Locate the Plasmodium falciparum-infected red blood cells and any of indeterminate infection status.
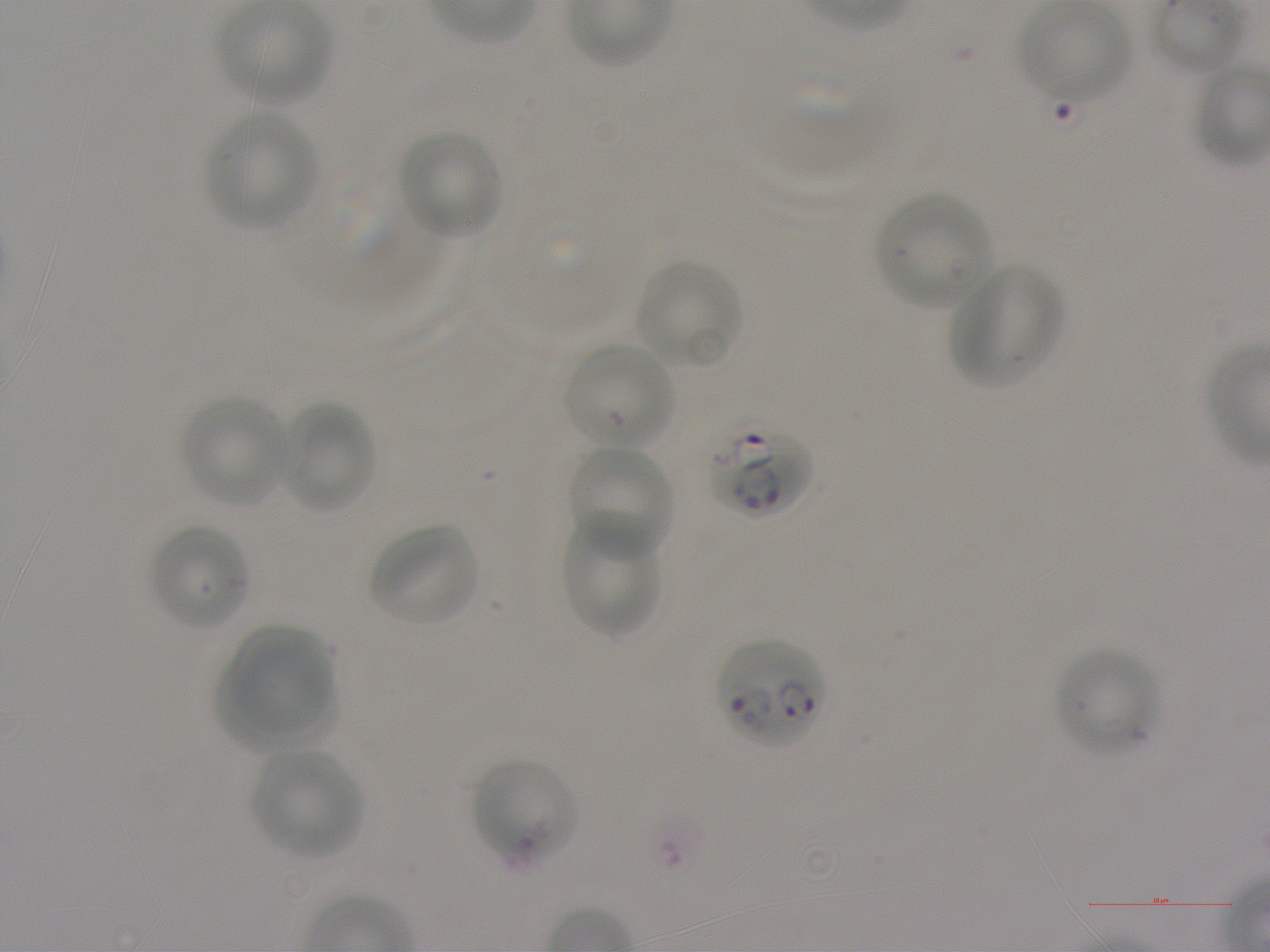
Approximate bounding rectangles given as corner coordinates in pixels from the top-left. Not every red blood cell is marked.
Infected red blood cells: (x1=706, y1=426, x2=813, y2=520), (x1=718, y1=639, x2=825, y2=750).
Red blood cells of indeterminate infection status: (x1=564, y1=344, x2=675, y2=451), (x1=472, y1=758, x2=578, y2=869).

Summary:
  - Locations of uninfected red blood cells: (x1=1019, y1=3, x2=1130, y2=104), (x1=217, y1=4, x2=329, y2=105), (x1=206, y1=112, x2=315, y2=231), (x1=397, y1=131, x2=501, y2=239), (x1=877, y1=193, x2=994, y2=309), (x1=635, y1=260, x2=743, y2=369), (x1=947, y1=266, x2=1064, y2=387), (x1=182, y1=396, x2=291, y2=507), (x1=280, y1=404, x2=377, y2=513), (x1=568, y1=441, x2=674, y2=560), (x1=564, y1=515, x2=661, y2=641), (x1=148, y1=523, x2=251, y2=631), (x1=369, y1=525, x2=480, y2=627), (x1=235, y1=626, x2=335, y2=732), (x1=1054, y1=648, x2=1158, y2=756), (x1=215, y1=653, x2=341, y2=755), (x1=254, y1=747, x2=363, y2=859)
  - Stain: Giemsa
  - Donor blood group: A+
  - Preparation: thin blood smear
  - Image size: 1270×952 pixels
  - Culture: static in-vitro Plasmodium falciparum strain NF54
  - Objective: 100x, oil immersion, numerical aperture 1.25
  - Field of view: single